Assess the morphology of the red blood cells.
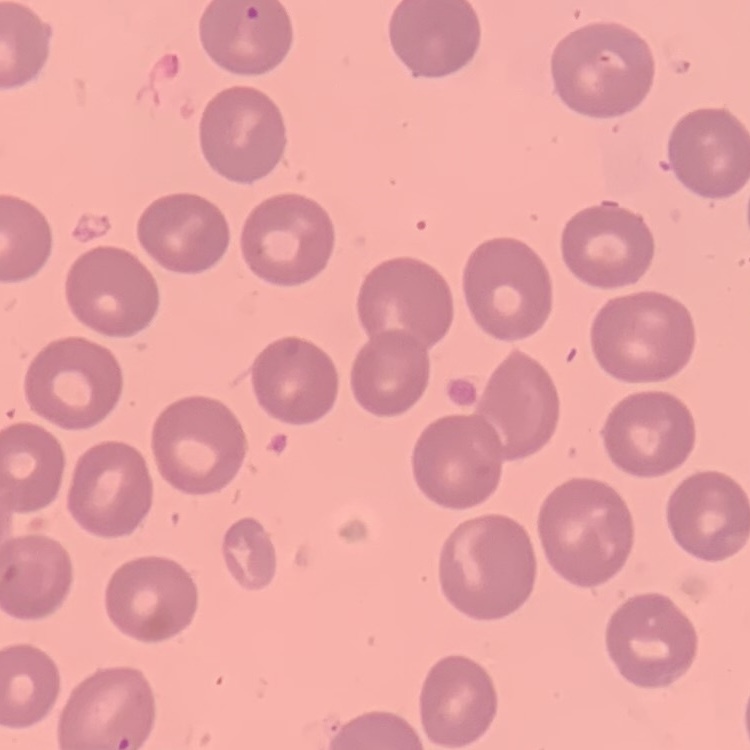

They show no rouleaux formation.

preparation = thin blood film
stain = Field's or Giemsa
image type = one tile cut from a larger photomicrograph